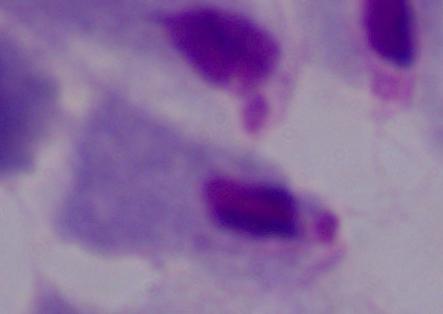
A trichomonad is shown. 1000x magnification. Photomicrograph.